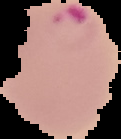
Summary:
  - Image type: segmented cell region with the area outside set to black
  - Result: Plasmodium parasites identified
  - Preparation: thin blood film
  - Image size: 121×139 pixels